Assess this cell for malaria.
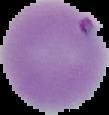

Parasitized.

preparation = thin blood smear
image size = 109×115 pixels
image type = segmented cell region with the area outside set to black